Give the position of every Plasmodium parasite.
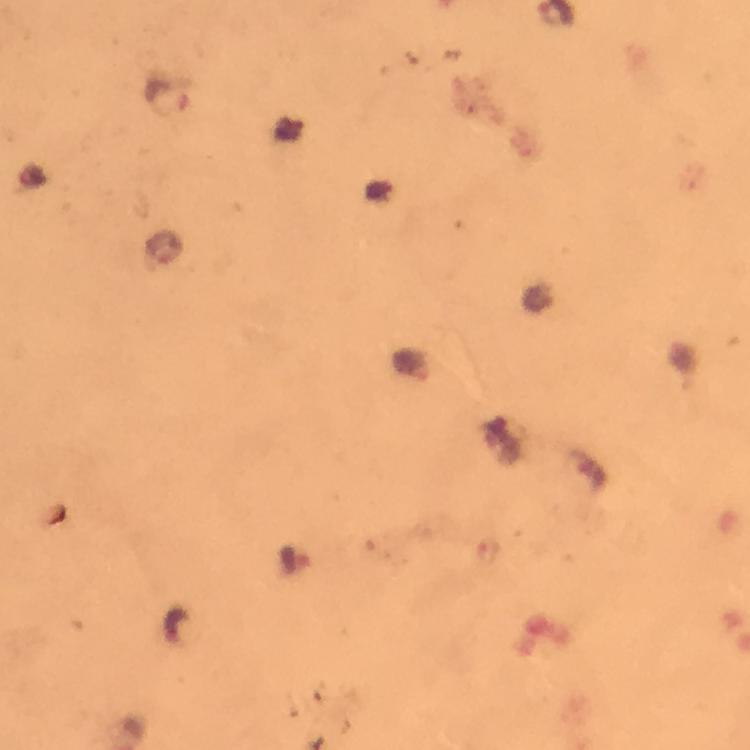
Approximate centers as (x, y) in pixels.
Plasmodium parasites: (294, 561).

immersion oil = used
cropped from = a single field of view
preparation = thick smear
magnification = 100x
context = from a malaria diagnostic workup
stain = Giemsa
capture = smartphone camera through the microscope
image size = 750×750 pixels